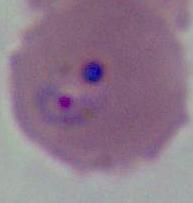 Micrograph. A Plasmodium parasite is seen. 400x or 1000x magnification.